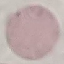 Malaria status: uninfected. Acquired by smartphone through the microscope eyepiece. Cell patch, automatically extracted from a larger field of view and resized to 64 × 64 pixels. Thin blood smear. Giemsa stain.